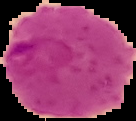
image type = segmented cell region on a black background
result = malaria parasites identified
preparation = thin blood smear
image size = 136×121 pixels